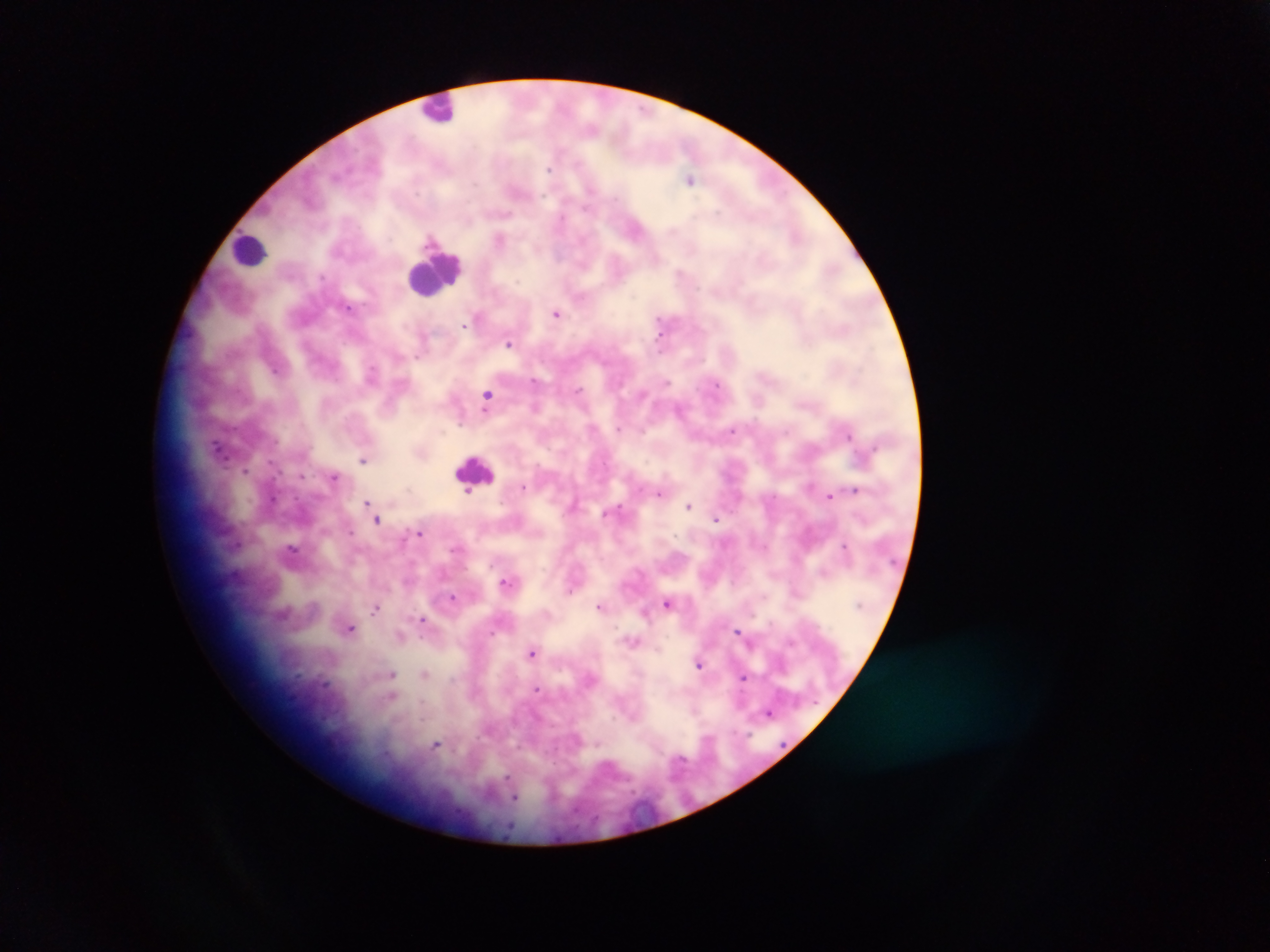
Approximate centers as x y in pixels.
Summary:
  - Leukocyte locations: 444 110; 244 251; 434 272
  - Malaria parasite locations: 550 169; 691 179; 475 185; 506 214; 499 238; 318 276; 348 307; 557 312; 658 319; 464 326; 659 334; 509 343; 276 370; 537 381; 669 383; 717 383; 577 389; 487 393; 679 410; 621 429; 734 432; 848 435; 218 447; 363 461; 244 470; 303 476; 334 476; 524 487; 854 488; 467 492; 660 494; 829 497; 369 501; 689 505; 718 518; 377 520; 421 532; 846 544; 505 580; 569 591; 455 598; 763 598; 668 606; 599 607; 375 609; 423 619; 352 628; 738 630; 658 648; 533 654; 700 663; 392 674; 425 674; 744 677; 537 688; 395 698; 694 711; 770 714; 708 737; 438 745; 679 758; 509 784; 513 798
  - Capture: mobile-phone photograph through a microscope
  - Field of view: single
  - Country: Ghana
  - Preparation: thick blood film
  - Image size: 1270×952 pixels